State which parasite is depicted.
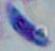
Toxoplasma gondii.

modality = photomicrograph
magnification = 1000x